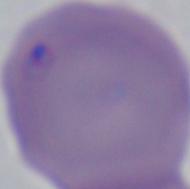
{
  "modality": "photomicrograph",
  "identification": "Babesia",
  "magnification": "1000x"
}